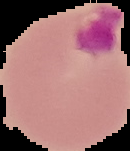
{
  "result": "malaria parasites identified",
  "preparation": "thin blood film",
  "image_size": "130×151 pixels",
  "image_type": "segmented cell region on a black background"
}